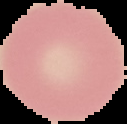

Summary:
  - Image type: segmented cell region on a black background
  - Malaria status: uninfected
  - Preparation: thin blood smear
  - Image size: 127×124 pixels